Describe the morphology of the red blood cells.
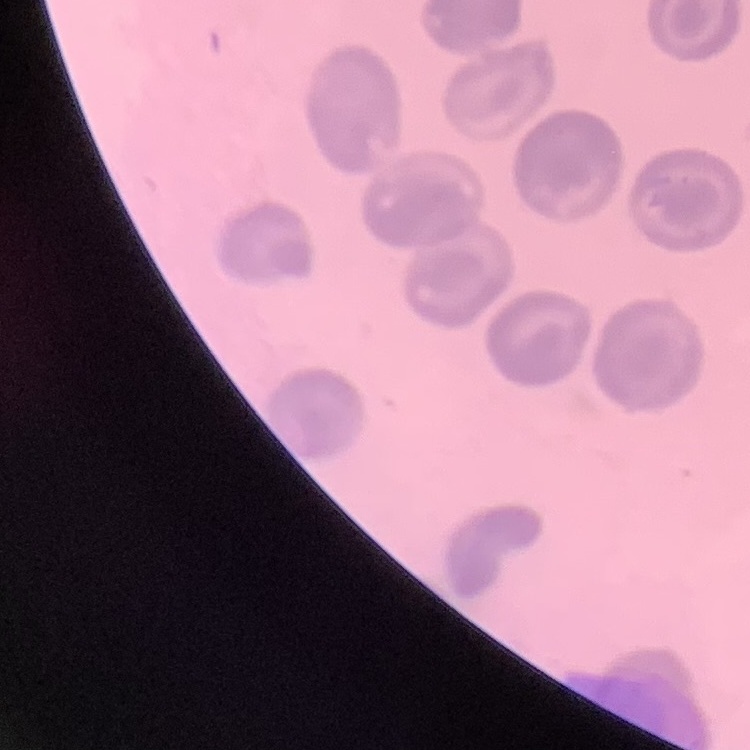
They show no rouleaux formation.

Summary:
  - Stain: Field's or Giemsa
  - Image type: one tile cut from a larger photomicrograph
  - Preparation: thin peripheral smear